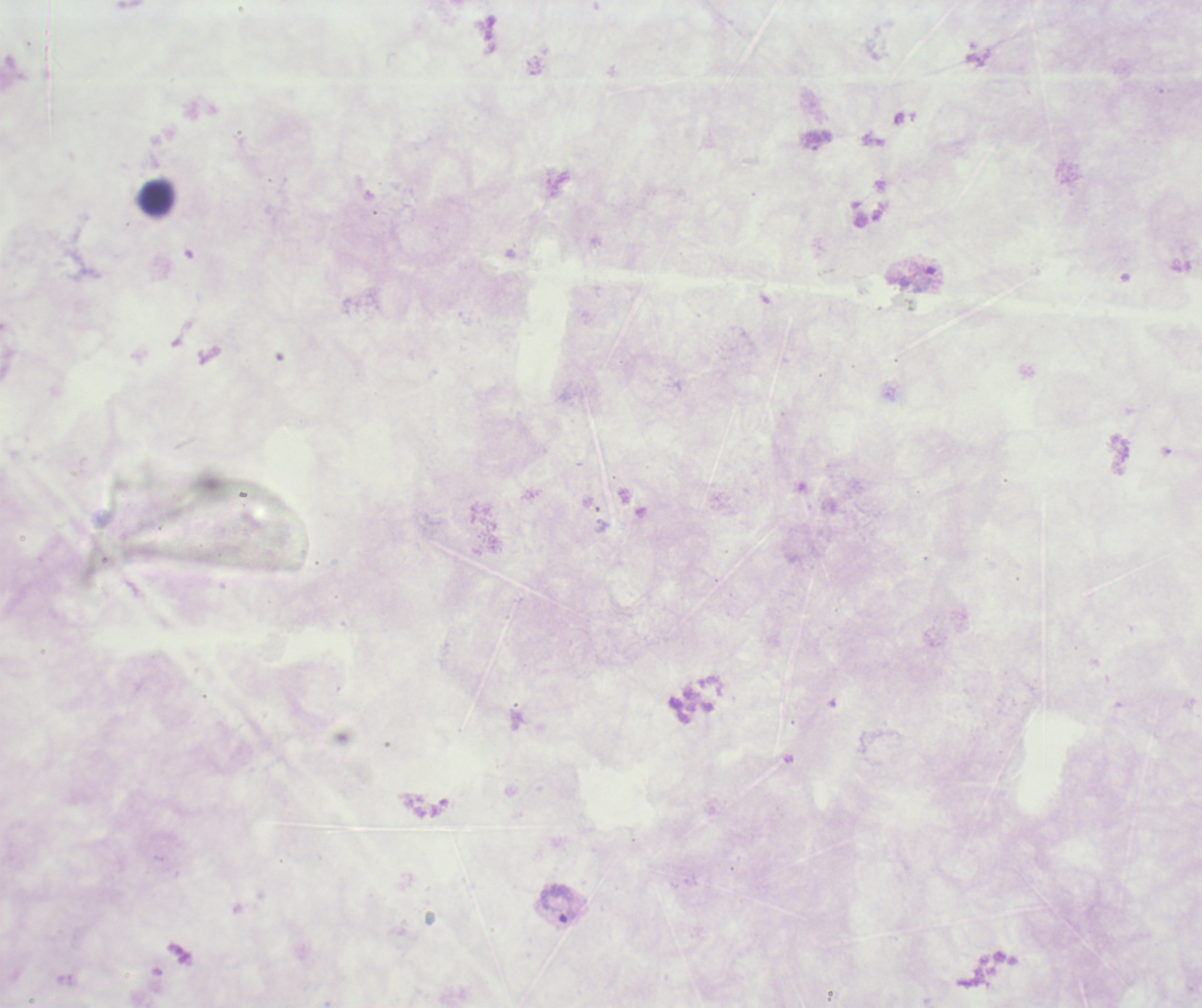

coordinate format = approximate centers as (x, y) in pixels
trophozoite locations = (924, 279), (559, 903)
leukocyte locations = (157, 197)
background quality = poor
coloration quality = bad
context = previously used in an actual diagnosis
result = Plasmodium parasites detected
field of view = one from this slide
stain = Romanowsky
preparation = thick smear of blood
image size = 1202×1008 pixels
magnification = 100x